Report the malaria status of this cell.
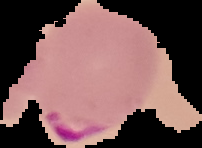

Parasitized.

Cell region segmented out of the field of view; the surrounding area is masked to black. Image is 202×148 pixels. From a thin blood film.